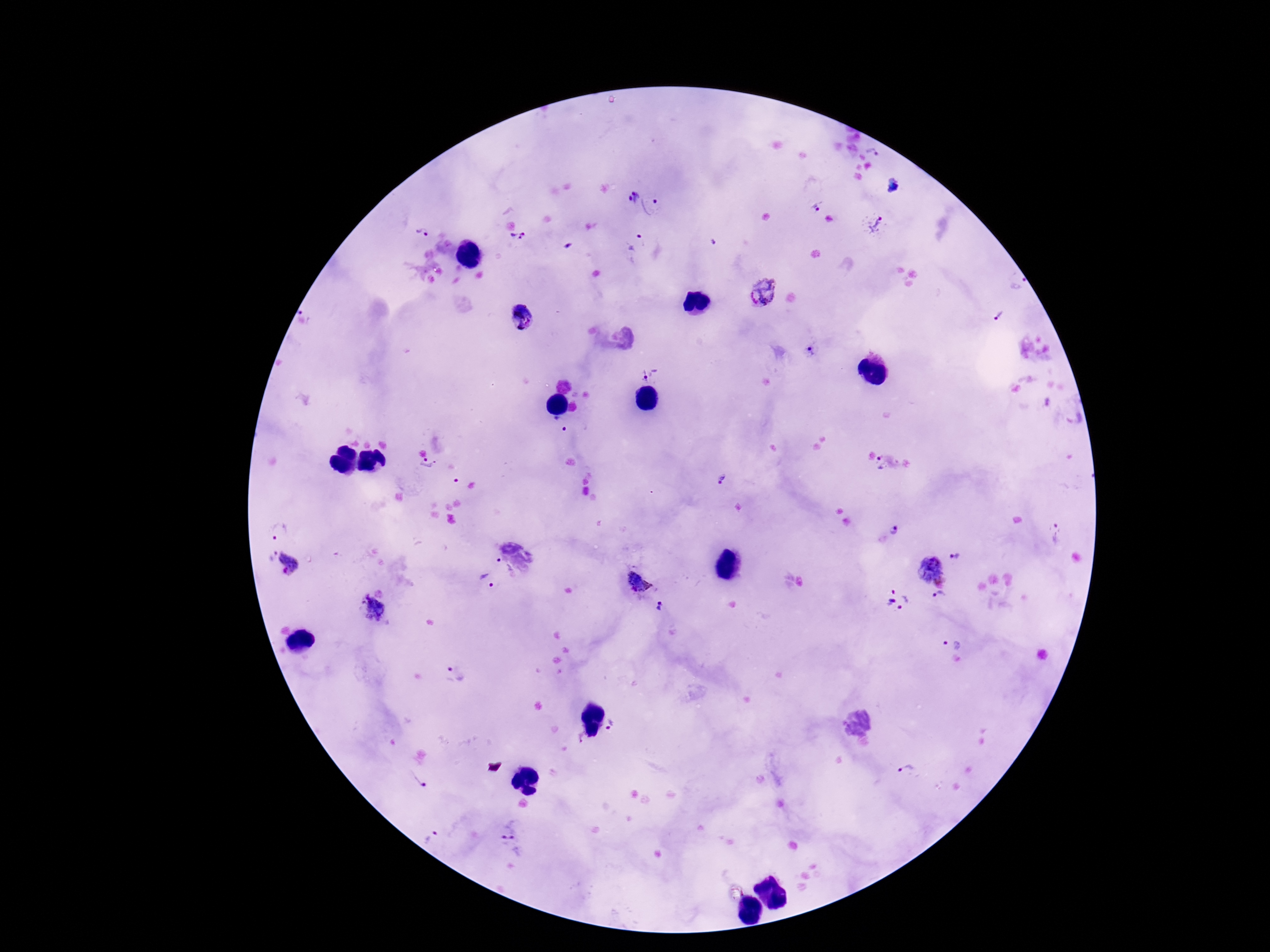

Approximate centers as (x, y) in pixels.
Summary:
  - Plasmodium parasite locations: (872, 152), (632, 196), (654, 201), (817, 205), (876, 224), (423, 233), (518, 241), (637, 242), (1019, 283), (763, 292), (1000, 315), (521, 317), (809, 350), (649, 371), (558, 423), (881, 463), (428, 466), (723, 479), (896, 529), (279, 531), (1056, 534), (272, 555), (955, 557), (289, 561), (499, 561), (931, 567), (487, 580), (638, 582), (939, 597), (898, 598), (372, 609), (661, 609), (951, 640), (455, 673), (617, 727), (578, 738), (906, 772), (418, 780), (509, 831), (432, 839)
  - Field of view: single
  - Capture: smartphone camera through the microscope eyepiece
  - Magnification: 100x
  - Patient malaria status: infected
  - Image size: 1270×952 pixels
  - Stain: Giemsa
  - Preparation: thick blood smear